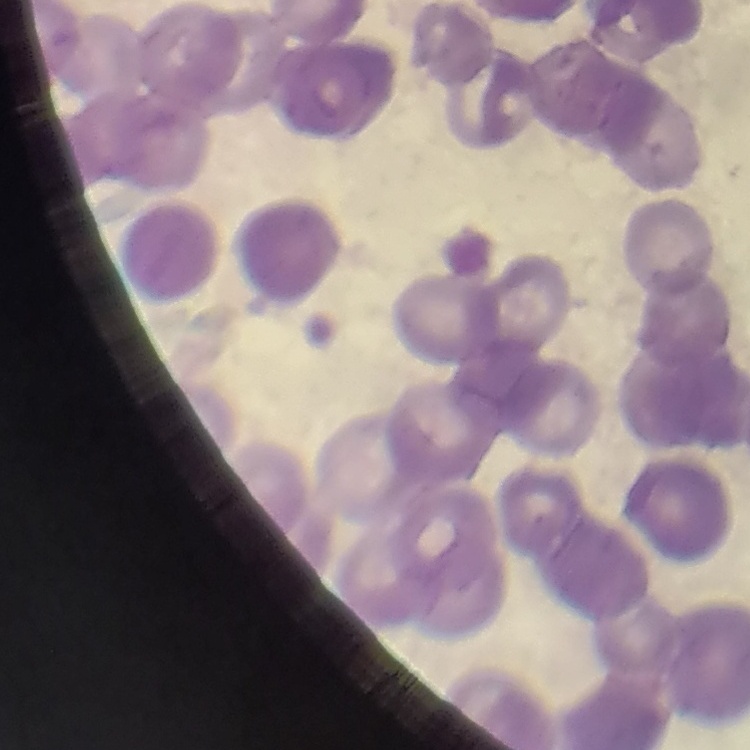

The red blood cells show rouleaux formation. Field's or Giemsa stain. Thin blood smear. Square crop of a larger photomicrograph.